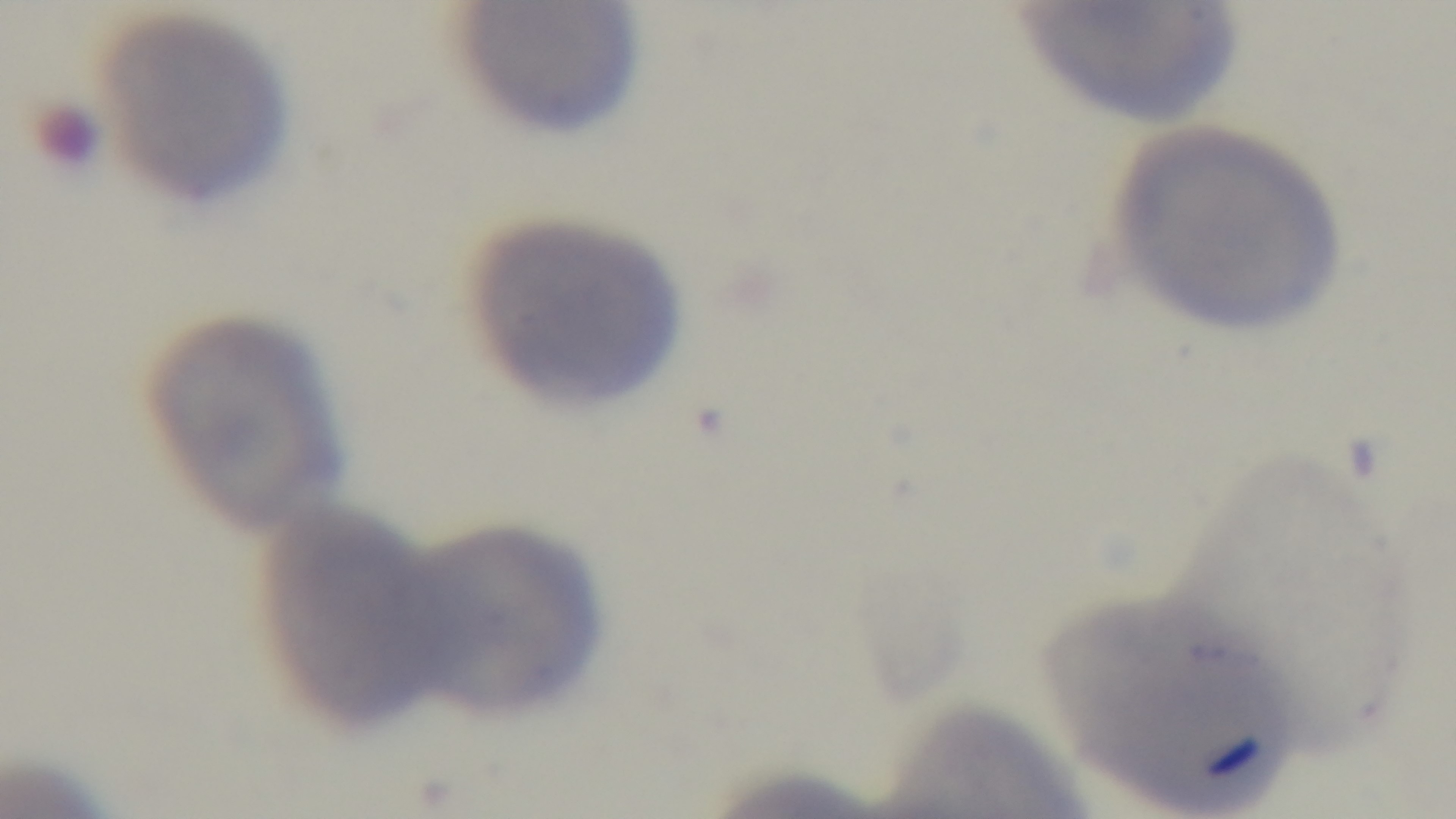

Summary:
  - Field of view: one from the slide
  - Modality: light microscopy
  - Objective: 100x oil immersion
  - Preparation: thin blood film
  - Malaria status: negative
  - Stain: Giemsa
  - Capture: mounted 4K digital camera